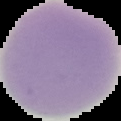 From a thin blood film. The area outside the segmented cell region is set to black. Image is 121×121 pixels. Result: negative for Plasmodium parasites.